Report the malaria status of this cell.
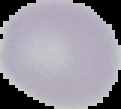
It is uninfected.

image size = 121×109 pixels
image type = segmented cell region with the area outside set to black
preparation = thin blood film